Give the extent of all uninfected red blood cells.
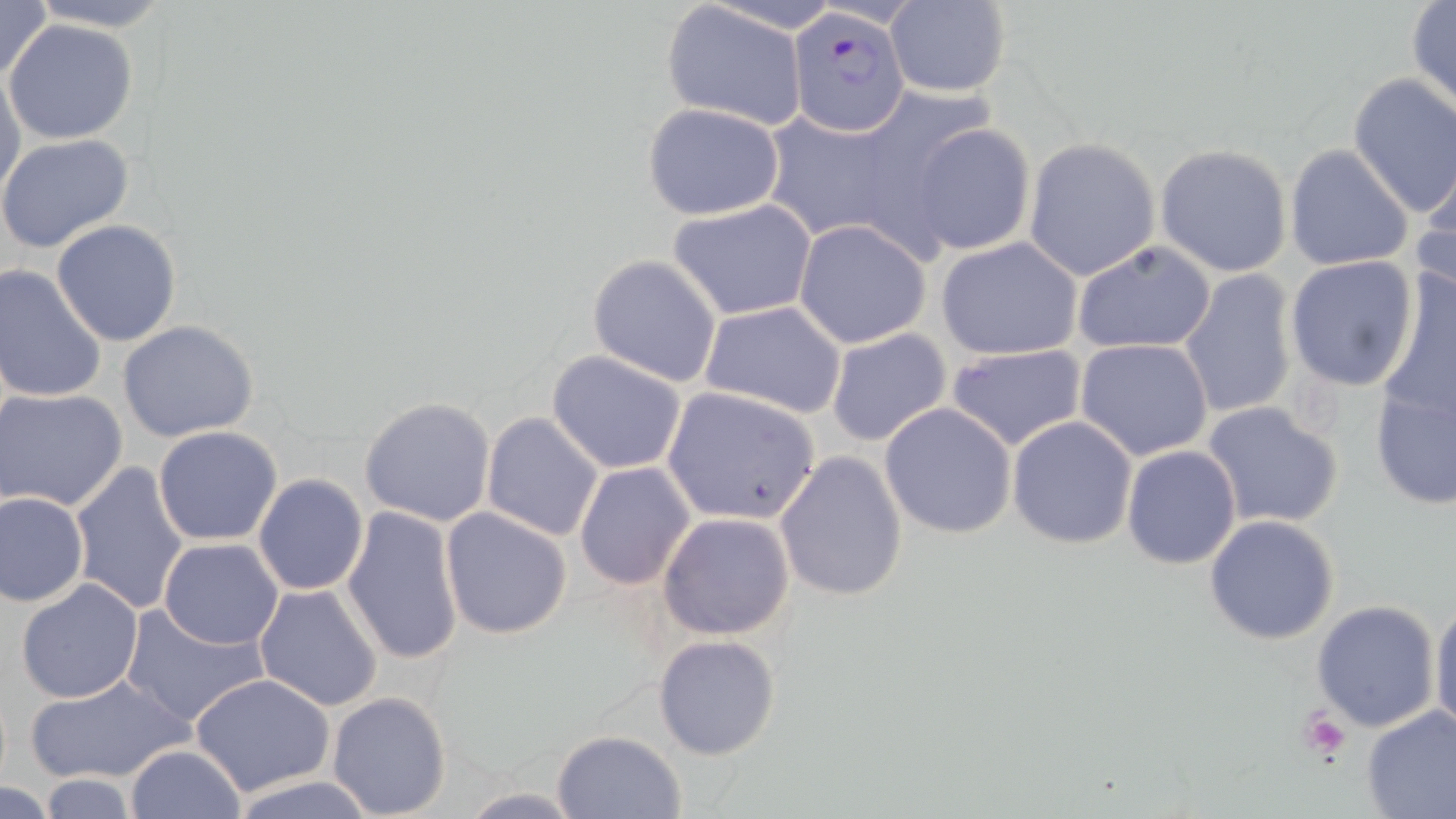

Approximate bounding boxes as (x1, y1, x2, y2) in pixels.
Uninfected red blood cells: (0, 0, 53, 87), (25, 0, 176, 30), (660, 2, 811, 131), (884, 2, 1013, 98), (1407, 3, 1456, 112), (6, 19, 138, 144), (1, 68, 26, 205), (1348, 73, 1456, 220), (641, 103, 787, 219), (760, 108, 912, 246), (909, 122, 1036, 256), (0, 134, 133, 255), (1023, 137, 1161, 282), (1284, 143, 1413, 273), (1155, 144, 1293, 277), (1412, 164, 1456, 307), (668, 198, 818, 322), (50, 219, 182, 348), (792, 220, 931, 349), (935, 237, 1084, 362), (1072, 240, 1217, 356), (587, 254, 723, 387), (1284, 255, 1421, 395), (1378, 263, 1456, 432), (0, 264, 107, 404), (1177, 269, 1298, 421), (700, 300, 848, 419), (117, 320, 262, 442), (825, 328, 952, 447), (1076, 339, 1216, 461), (945, 342, 1088, 453), (546, 349, 688, 474), (1369, 370, 1456, 513), (661, 386, 822, 527), (1, 388, 129, 513), (358, 395, 497, 526), (879, 402, 1020, 539), (1201, 402, 1344, 530), (481, 411, 605, 543), (1006, 416, 1137, 548), (153, 425, 284, 546), (1121, 445, 1242, 569), (775, 451, 908, 602), (70, 460, 190, 615), (574, 461, 697, 589), (253, 473, 369, 596), (1, 491, 89, 607), (341, 506, 465, 665), (440, 506, 573, 640), (658, 512, 794, 641), (1204, 515, 1341, 646), (158, 538, 285, 650), (14, 579, 144, 703), (253, 584, 385, 714), (1429, 594, 1456, 737), (1310, 599, 1441, 732), (120, 602, 267, 728), (653, 634, 780, 759), (25, 671, 191, 785), (190, 672, 338, 795), (326, 690, 452, 817), (1359, 703, 1456, 819), (553, 730, 687, 817), (125, 743, 248, 818), (229, 774, 380, 818), (35, 775, 139, 817), (0, 781, 58, 816), (452, 788, 591, 817).

Plasmodium falciparum-infected red blood cell locations = approximate bounding boxes as (x1, y1, x2, y2) in pixels: (787, 10, 911, 136)
slide-level diagnosis = Plasmodium falciparum
field of view = single
platelet locations = approximate bounding boxes as (x1, y1, x2, y2) in pixels: (1296, 707, 1353, 764)
preparation = thin blood film
magnification = 1000x
stain = May-Grünwald-Giemsa
modality = optical microscopy
image size = 1456×819 pixels